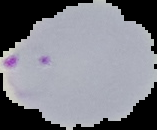
The area outside the segmented cell region is set to black. Result: Plasmodium parasites detected. From a thin blood smear. Image is 157×130 pixels.